Name the blood parasite species.
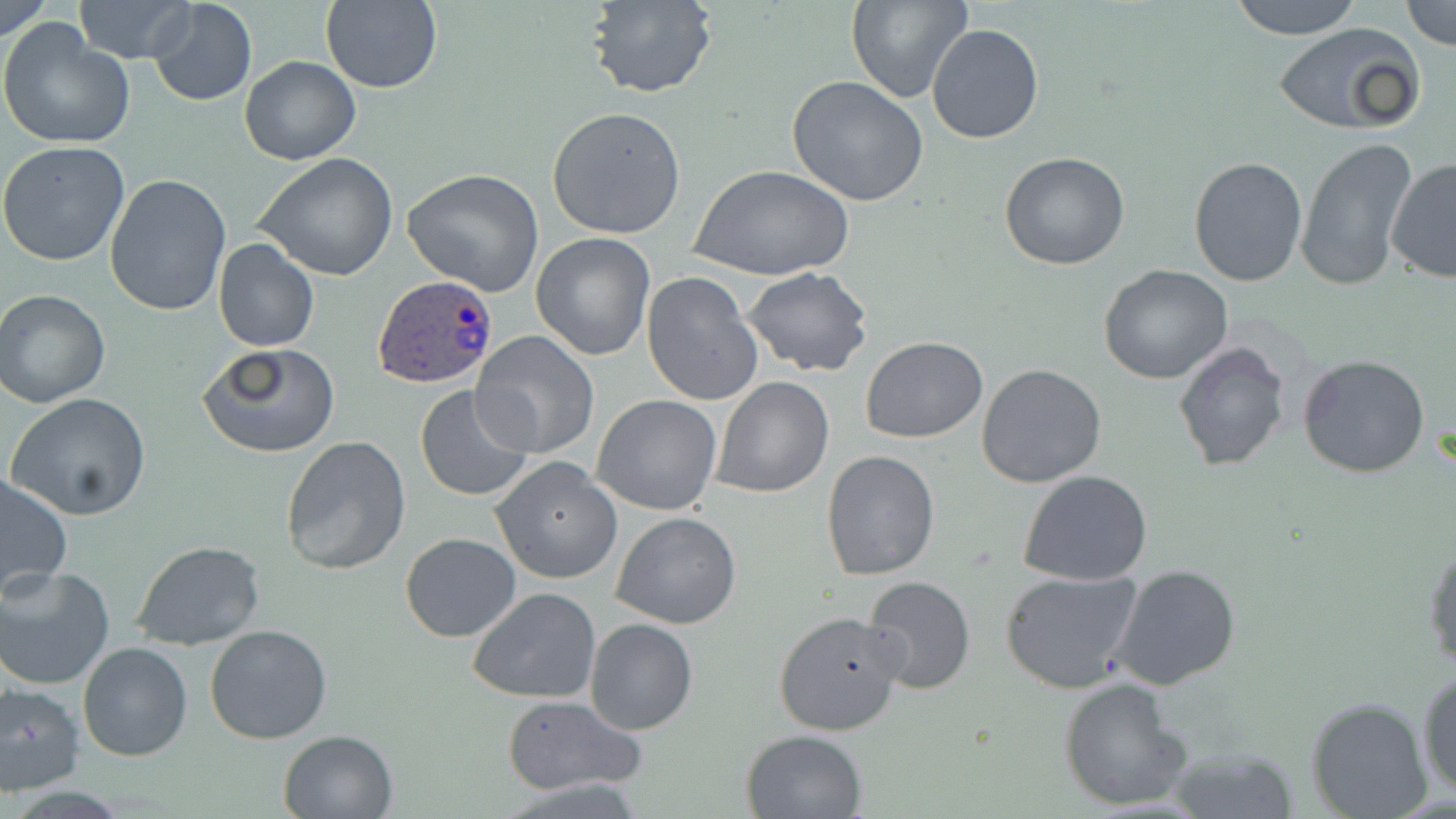

Plasmodium ovale.

Approximate bounding boxes as (x1,y1)-(x2,y2) corner pairs in pixels. Plasmodium ovale-infected red blood cell locations: (375,274)-(497,387). Uninfected red blood cell locations: (0,0)-(51,46), (74,0)-(194,65), (148,0)-(256,107), (584,0)-(717,99), (846,0)-(972,105), (1230,0)-(1364,38), (319,1)-(443,92), (1400,2)-(1456,49), (0,20)-(134,149), (1272,20)-(1427,136), (927,22)-(1044,143), (240,55)-(360,165), (786,75)-(930,207), (547,106)-(687,240), (1295,138)-(1420,294), (0,140)-(130,266), (999,152)-(1131,271), (255,154)-(400,282), (1188,155)-(1307,286), (1385,157)-(1456,285), (693,164)-(851,282), (402,168)-(547,297), (104,175)-(231,317), (228,177)-(370,343), (529,232)-(656,360), (213,239)-(319,352), (1098,265)-(1236,385), (743,268)-(873,379), (641,271)-(764,408), (0,288)-(114,407), (472,332)-(599,460), (860,337)-(988,442), (1173,341)-(1291,472), (197,343)-(341,459), (1298,353)-(1431,478), (976,363)-(1107,487), (710,377)-(834,498), (412,383)-(535,504), (6,393)-(152,519), (592,395)-(722,515), (280,435)-(412,577), (821,449)-(941,579), (491,456)-(622,585), (1018,471)-(1153,587), (0,472)-(74,598), (611,511)-(742,630), (400,531)-(521,642), (1423,533)-(1456,672), (133,540)-(266,650), (1109,563)-(1242,690), (0,565)-(115,690), (999,568)-(1144,692), (863,575)-(975,693), (467,587)-(602,703), (772,609)-(907,737), (584,619)-(699,735), (204,624)-(333,743), (78,642)-(194,763), (1416,665)-(1456,801), (1058,677)-(1192,812), (0,682)-(84,794), (500,695)-(646,797), (1303,696)-(1434,819), (278,728)-(400,818), (741,728)-(867,818), (1165,746)-(1300,818). Captured at 1000x magnification. Optical microscopy. Thin blood film. Image is 1456×819 pixels. May-Grünwald-Giemsa-stained preparation. One field of a larger specimen.